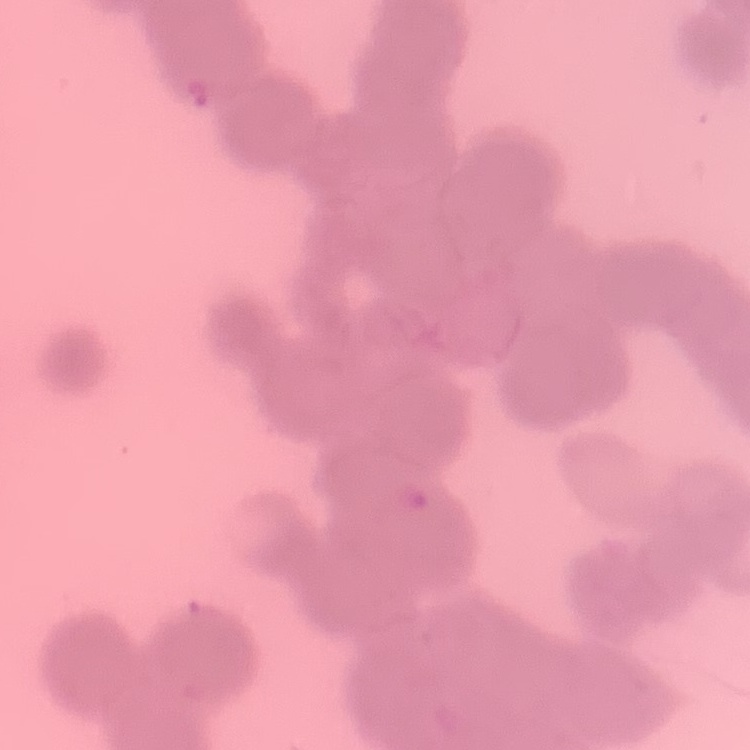

Summary:
  - Red blood cell morphology: rouleaux formation
  - Stain: Field's or Giemsa
  - Image type: square crop of a larger photomicrograph
  - Preparation: thin peripheral smear